Classify this cell by malaria status.
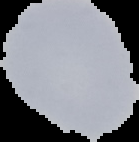

It is uninfected.

image_type: segmented cell region on a black background
preparation: thin blood smear
image_size: 139×142 pixels